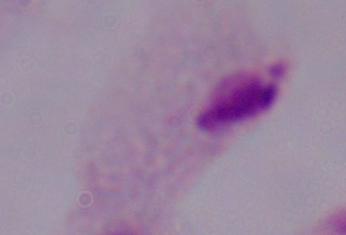

modality = micrograph
identification = trichomonad
magnification = 1000x